Assess for malaria.
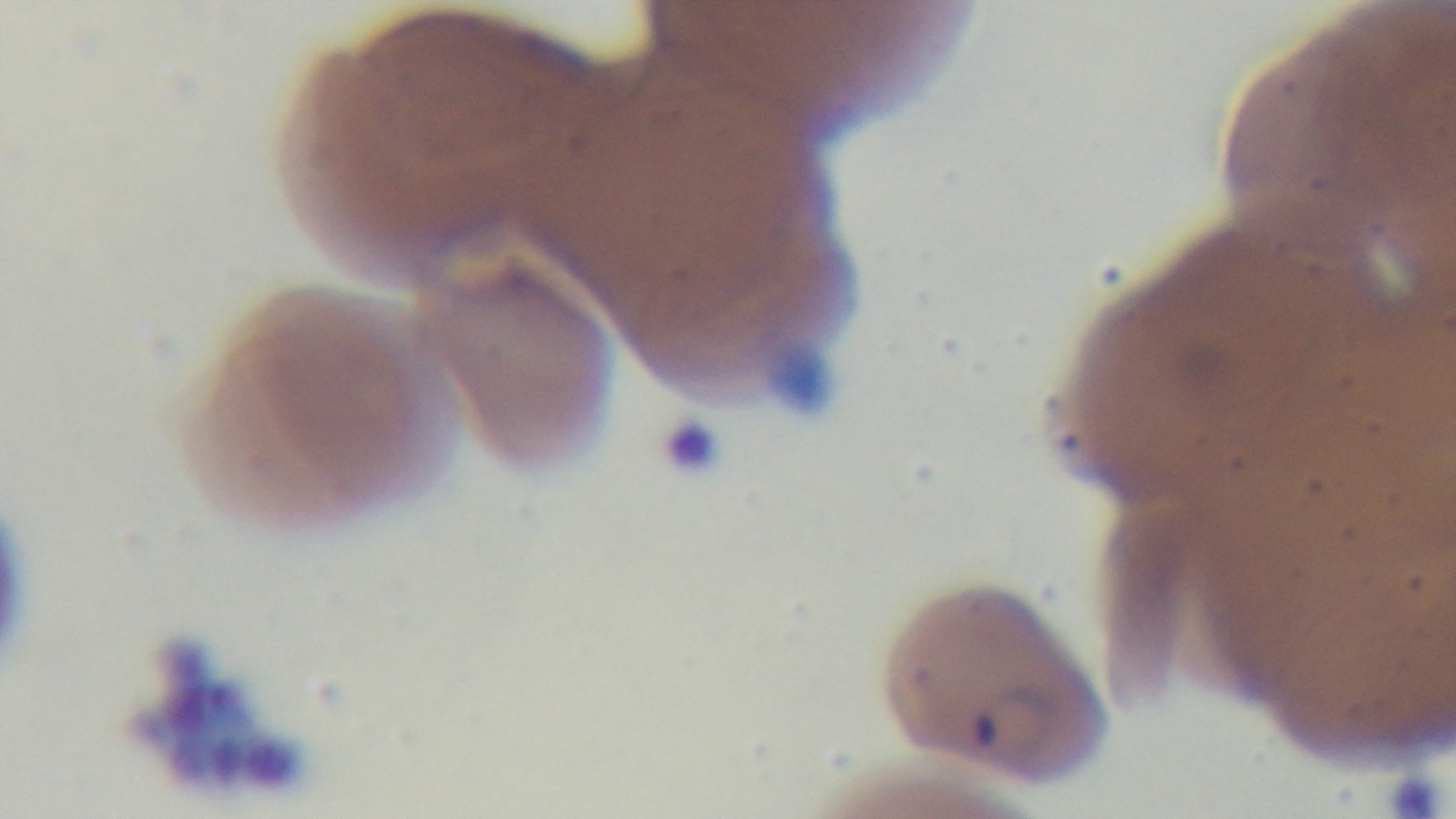

Positive.

field of view = one from the slide
modality = light microscopy
objective = 100x oil immersion
preparation = thin smear
capture = mounted 4K digital camera
stain = Giemsa